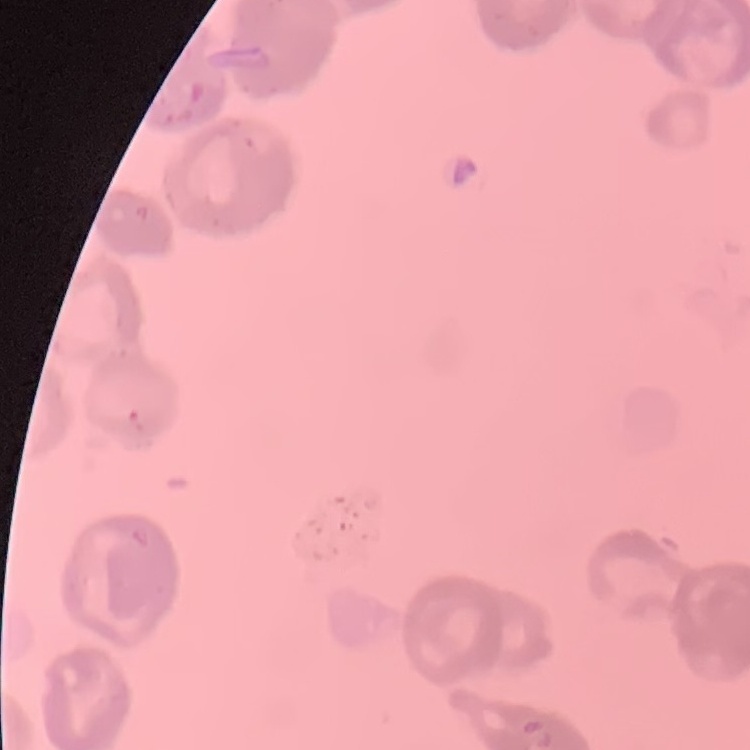

The red blood cells show rouleaux formation. Thin peripheral smear. Field's or Giemsa stain. One tile cut from a larger photomicrograph.